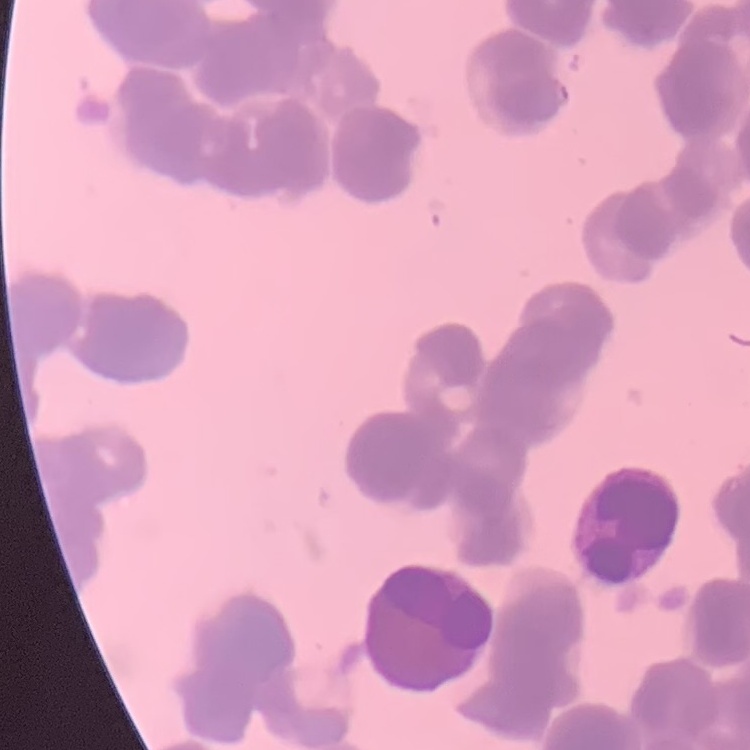

The red blood cells show rouleaux formation. Thin blood smear. Stained with either Field's or Giemsa. One tile cut from a larger photomicrograph.